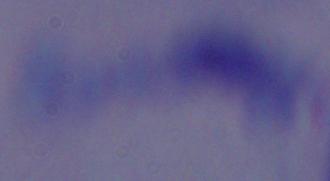
modality = photomicrograph
identification = trypanosome
magnification = 1000x